Identify the preparation type.
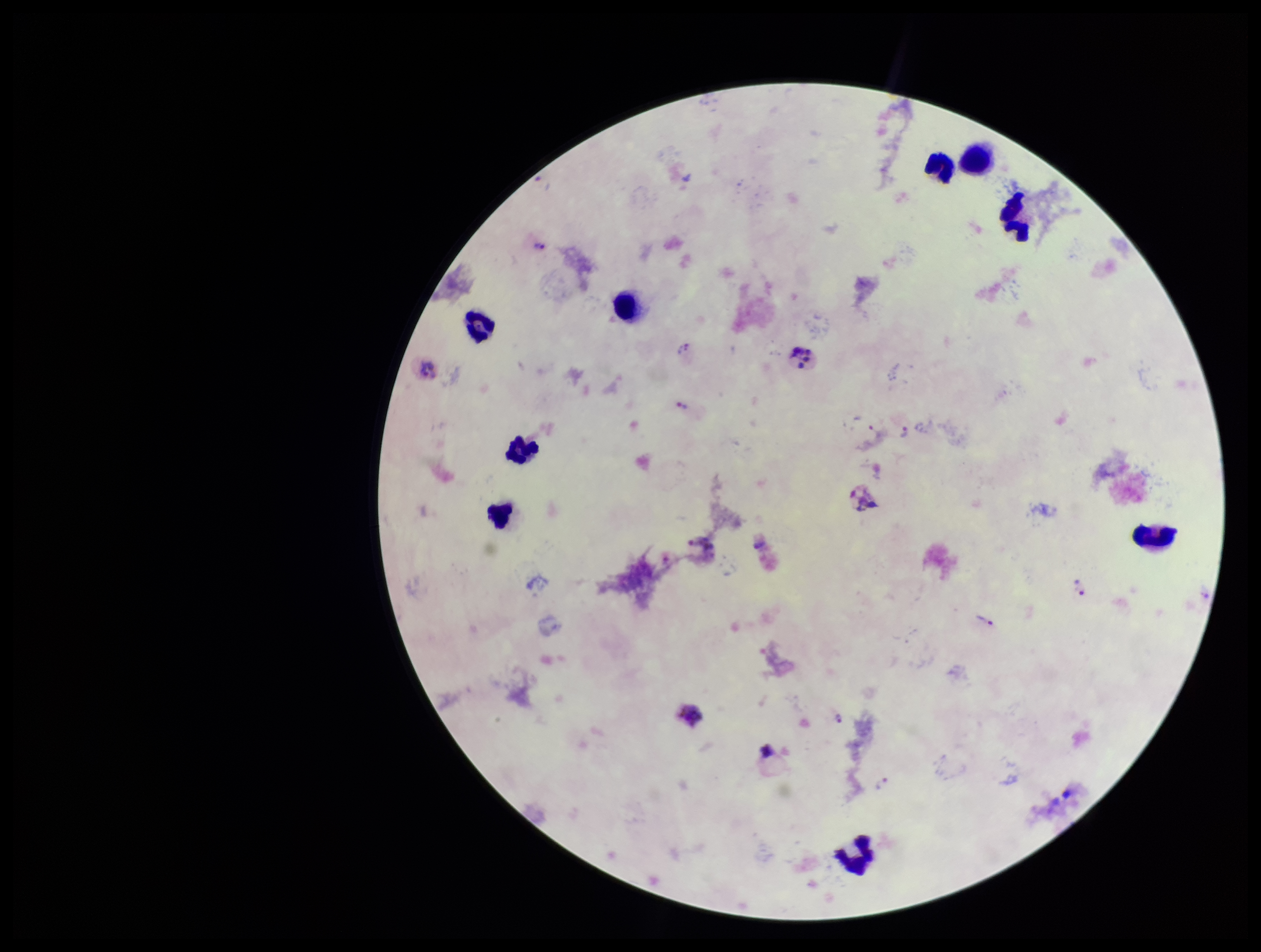
It is a thick blood smear.

Summary:
  - Species reported for this patient: Plasmodium vivax
  - Patient malaria status: infected
  - Plasmodium parasites: detected
  - Stain: Giemsa
  - Parasite count: 4
  - Capture: smartphone photograph through the microscope eyepiece
  - Leukocyte count: 9
  - Image size: 1261×952 pixels
  - Field of view: one from this slide